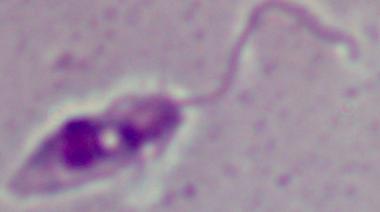
Summary:
  - Modality: micrograph
  - Identification: Leishmania
  - Magnification: 1000x